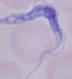

Summary:
  - Identification: trypanosome
  - Magnification: 1000x
  - Modality: micrograph